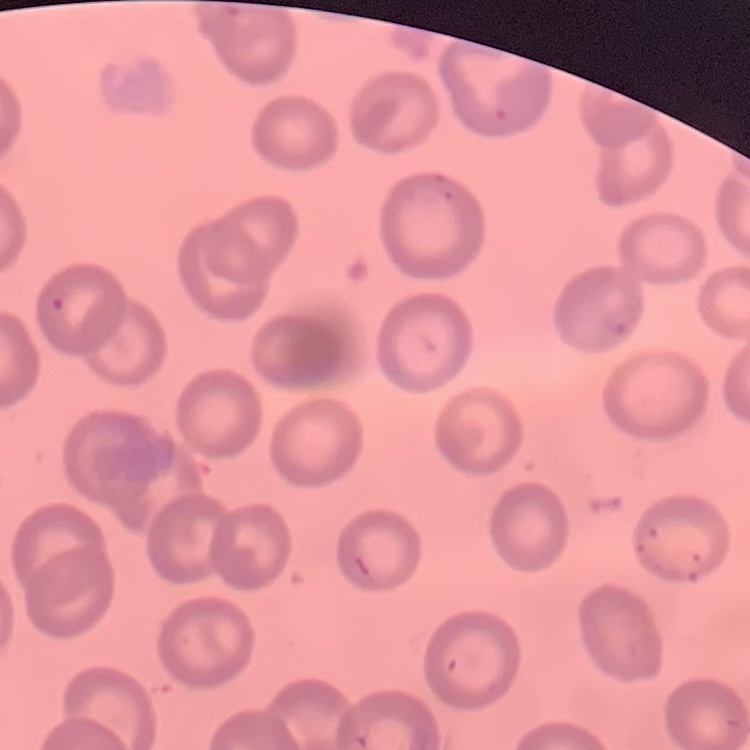

The red blood cells exhibit no rouleaux formation. Square crop of a larger photomicrograph. Field's or Giemsa stain. Thin blood film.